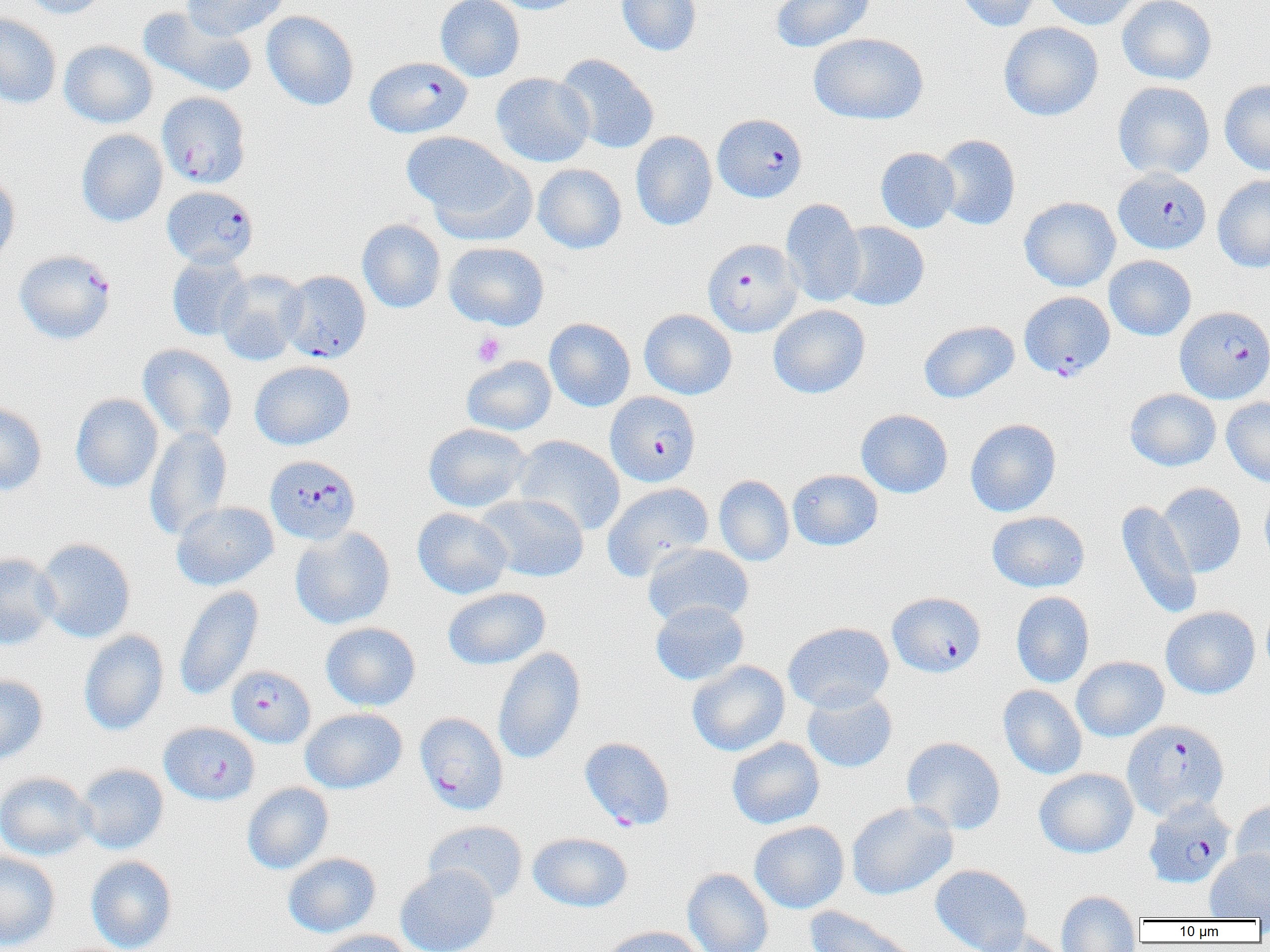

Approximate bounding boxes as (x1, y1, x2, y2) in pixels. Platelet locations: (472, 332, 505, 367). Uninfected red blood cell locations (subset): (19, 0, 111, 19), (183, 0, 288, 41), (435, 0, 525, 82), (486, 0, 587, 14), (616, 0, 702, 56), (771, 0, 875, 52), (956, 0, 1043, 32), (1041, 0, 1143, 30), (1117, 0, 1216, 85), (138, 6, 258, 97), (261, 11, 359, 110), (0, 13, 62, 109), (998, 22, 1104, 121), (809, 33, 929, 125), (59, 40, 157, 128), (555, 53, 659, 154), (491, 73, 594, 167), (1220, 79, 1270, 175), (1113, 81, 1215, 180), (76, 129, 167, 227), (630, 131, 717, 231), (402, 132, 521, 225), (933, 134, 1020, 230), (875, 147, 959, 233), (425, 157, 537, 248), (533, 164, 627, 253), (0, 167, 20, 267), (1213, 174, 1270, 273), (1020, 197, 1120, 291), (780, 198, 866, 307), (357, 219, 446, 313), (835, 221, 929, 311), (443, 242, 549, 330), (166, 253, 252, 341), (1104, 255, 1196, 341), (216, 270, 307, 365), (768, 304, 870, 399), (639, 309, 737, 399), (544, 318, 635, 411), (918, 320, 1019, 403), (138, 344, 237, 443), (461, 356, 556, 435), (249, 360, 355, 450), (1125, 389, 1221, 471), (70, 393, 164, 493), (1221, 397, 1270, 487), (0, 401, 47, 496), (856, 409, 953, 498), (965, 418, 1061, 517), (423, 423, 531, 513), (145, 426, 233, 540), (512, 435, 626, 535), (788, 469, 882, 550), (714, 475, 794, 566), (602, 482, 714, 581), (1158, 482, 1246, 577), (1259, 485, 1270, 572), (475, 493, 589, 582), (1115, 500, 1202, 619), (171, 501, 278, 590), (412, 507, 512, 599), (987, 511, 1090, 592), (289, 526, 395, 630), (36, 538, 136, 643), (643, 543, 753, 627), (0, 552, 60, 650), (174, 586, 264, 701), (442, 587, 550, 669), (1010, 591, 1095, 688), (650, 601, 748, 685), (1161, 606, 1260, 699), (320, 622, 421, 711), (783, 622, 894, 713), (79, 630, 169, 735), (492, 646, 586, 765), (1071, 656, 1168, 742), (687, 660, 790, 756), (0, 674, 48, 765), (998, 685, 1087, 780), (802, 687, 898, 773), (300, 707, 407, 794), (901, 736, 1006, 835), (726, 737, 825, 829), (75, 763, 169, 854), (1035, 768, 1138, 858), (0, 771, 95, 861), (242, 782, 333, 874), (1230, 800, 1270, 891), (846, 801, 958, 900), (424, 820, 528, 905), (749, 821, 849, 913), (528, 832, 633, 912), (1205, 850, 1270, 920), (0, 851, 61, 950), (283, 852, 381, 937), (86, 856, 177, 952), (395, 864, 499, 952), (930, 864, 1032, 952), (682, 867, 773, 952), (1056, 890, 1142, 952), (804, 906, 923, 952), (598, 926, 707, 952), (973, 928, 1068, 952), (315, 929, 416, 952). Plasmodium falciparum-infected red blood cell locations (subset): (364, 56, 472, 138), (157, 92, 251, 188), (713, 113, 807, 203), (1114, 168, 1212, 254), (162, 186, 258, 269), (703, 239, 802, 337), (14, 250, 116, 344), (281, 270, 371, 362), (1019, 291, 1115, 381), (1174, 306, 1270, 403), (605, 391, 700, 487), (265, 455, 360, 544), (887, 592, 986, 677), (226, 665, 315, 747), (414, 712, 509, 815), (1122, 720, 1229, 821), (159, 722, 260, 805), (1144, 799, 1235, 888). Slide-level diagnosis: Plasmodium falciparum. Thin blood film. Optical microscopy. 1000x magnification. Image is 1270×952 pixels. Single field of view.